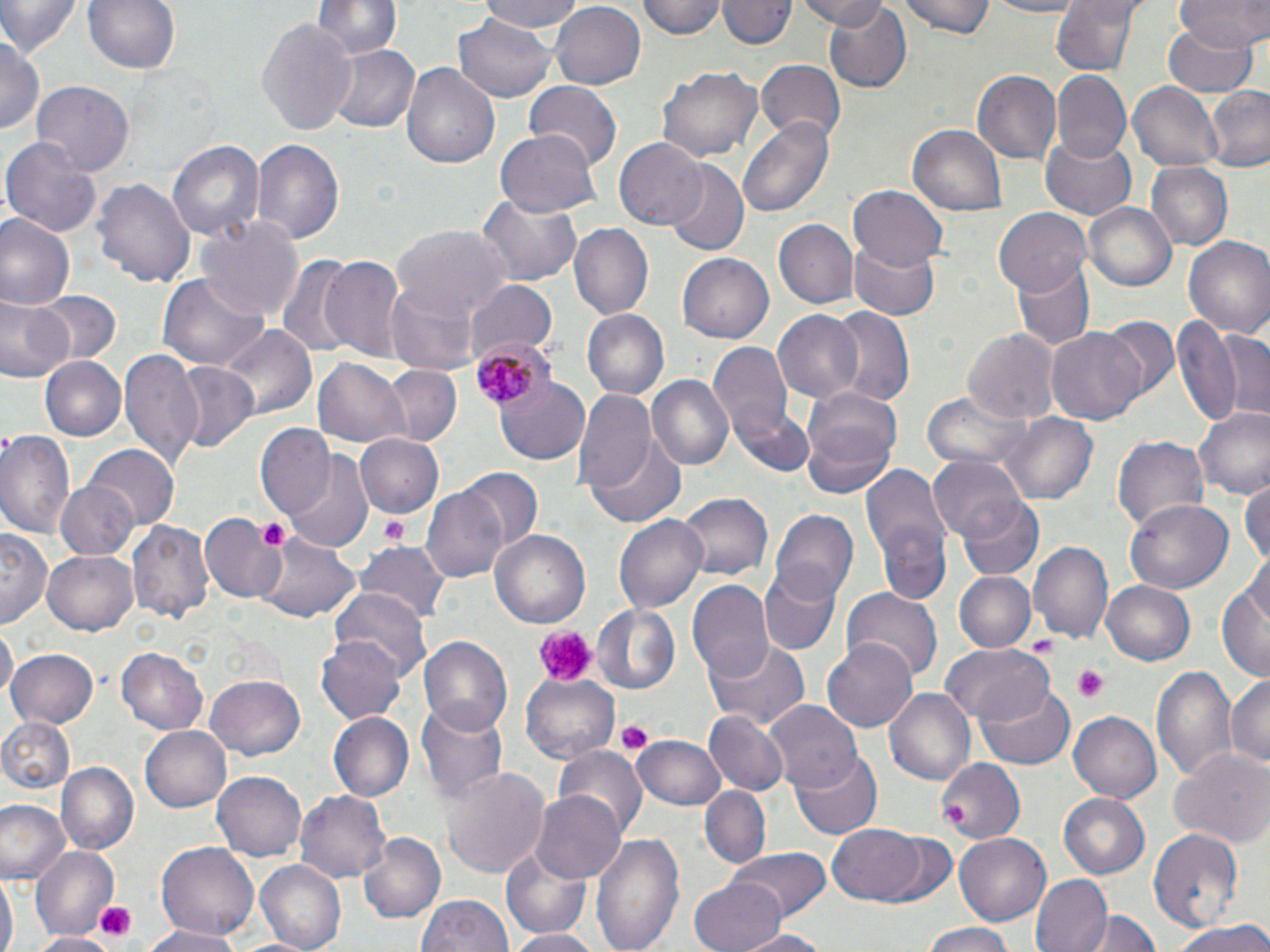

Summary:
  - Coordinate format: approximate bounding boxes as (x1, y1, x2, y2) in pixels
  - Plasmodium malariae-infected red blood cell locations: (468, 336, 555, 414)
  - Platelet locations: (379, 514, 409, 544), (258, 518, 292, 551), (531, 624, 597, 689), (1072, 665, 1112, 702), (615, 718, 651, 753), (939, 802, 964, 826), (93, 901, 136, 943)
  - Uninfected red blood cell locations: (0, 0, 81, 59), (83, 0, 182, 78), (478, 0, 588, 32), (549, 0, 645, 87), (640, 0, 727, 39), (793, 0, 896, 29), (819, 0, 912, 91), (900, 0, 997, 40), (984, 0, 1086, 18), (1053, 0, 1139, 78), (1178, 0, 1269, 48), (313, 1, 400, 62), (719, 1, 792, 52), (452, 13, 555, 102), (258, 19, 356, 135), (1161, 22, 1258, 94), (0, 34, 43, 138), (326, 42, 418, 134), (400, 60, 502, 169), (755, 61, 846, 144), (656, 66, 763, 164), (973, 70, 1064, 166), (1051, 72, 1129, 165), (32, 80, 136, 175), (523, 80, 621, 172), (1128, 80, 1225, 173), (1202, 86, 1270, 173), (737, 117, 835, 219), (909, 124, 1007, 218), (496, 127, 599, 217), (1040, 133, 1139, 218), (4, 134, 103, 238), (167, 137, 264, 244), (249, 137, 344, 248), (614, 138, 707, 230), (663, 161, 749, 253), (1147, 164, 1232, 249), (95, 175, 193, 290), (849, 186, 948, 270), (477, 195, 582, 287), (1085, 202, 1175, 292), (993, 208, 1091, 295), (0, 215, 74, 310), (195, 216, 305, 323), (773, 219, 859, 310), (567, 223, 653, 318), (393, 225, 512, 318), (1182, 235, 1270, 338), (849, 238, 940, 319), (676, 253, 772, 342), (275, 255, 358, 358), (321, 256, 407, 364), (1010, 258, 1094, 350), (158, 273, 268, 371), (387, 282, 483, 375), (466, 283, 559, 363), (34, 289, 118, 365), (0, 295, 72, 386), (827, 304, 915, 407), (580, 310, 670, 401), (772, 310, 865, 404), (1099, 317, 1180, 404), (1173, 317, 1247, 428), (218, 325, 315, 417), (1045, 325, 1146, 426), (961, 327, 1058, 426), (1214, 327, 1269, 424), (709, 343, 794, 443), (120, 350, 205, 470), (313, 356, 409, 448), (41, 357, 126, 441), (171, 363, 259, 455), (379, 364, 462, 447), (646, 374, 734, 472), (493, 376, 591, 466), (574, 390, 656, 497), (801, 391, 900, 498), (924, 391, 1029, 474), (728, 402, 815, 481), (1194, 406, 1270, 502), (997, 412, 1101, 505), (254, 425, 334, 519), (0, 428, 78, 543), (1112, 432, 1210, 533), (355, 434, 445, 518), (587, 434, 688, 528), (86, 445, 180, 532), (284, 454, 373, 554), (929, 456, 1027, 544), (861, 462, 951, 585), (457, 468, 542, 555), (1241, 477, 1270, 567), (56, 480, 140, 560), (421, 484, 513, 587), (674, 492, 770, 582), (958, 495, 1044, 581), (1126, 499, 1233, 596), (770, 509, 858, 607), (202, 514, 286, 603), (613, 515, 708, 614), (126, 517, 214, 624), (874, 521, 952, 608), (491, 527, 593, 629), (0, 528, 52, 624), (256, 535, 359, 625), (1028, 542, 1114, 646), (358, 544, 451, 628), (44, 551, 136, 635), (1220, 563, 1269, 684), (758, 565, 842, 656), (953, 571, 1035, 654), (1102, 580, 1195, 666), (687, 581, 775, 680), (843, 585, 942, 684), (332, 586, 431, 677), (592, 603, 681, 694), (2, 625, 17, 700), (316, 634, 406, 725), (705, 636, 811, 731), (418, 637, 513, 735), (822, 637, 917, 733), (940, 642, 1054, 724), (7, 646, 100, 731), (116, 648, 208, 735), (1151, 665, 1238, 780), (520, 671, 620, 764), (1226, 672, 1269, 773), (205, 676, 307, 759), (975, 682, 1074, 770), (885, 689, 975, 786), (416, 699, 508, 801), (764, 699, 863, 794), (706, 710, 788, 795), (1069, 711, 1161, 802), (327, 713, 414, 802), (0, 718, 76, 794), (140, 725, 233, 812), (632, 734, 727, 810), (554, 744, 645, 836), (1169, 747, 1270, 848), (791, 752, 882, 839), (935, 758, 1025, 845), (58, 761, 137, 852), (441, 768, 549, 876), (211, 771, 307, 861), (697, 787, 772, 870), (296, 789, 390, 886), (530, 790, 626, 884), (1057, 792, 1150, 881), (0, 799, 67, 882), (829, 823, 927, 904), (1148, 827, 1244, 929), (360, 830, 445, 924), (869, 830, 961, 909), (589, 833, 684, 952), (956, 834, 1050, 922), (155, 843, 260, 940), (32, 846, 118, 936), (728, 847, 833, 921), (499, 849, 592, 940), (254, 861, 345, 950), (1, 874, 16, 952), (1029, 874, 1112, 952), (688, 875, 785, 952), (415, 893, 515, 952), (1091, 910, 1161, 952), (1167, 921, 1270, 952), (922, 922, 1015, 952), (143, 927, 250, 951), (731, 928, 835, 951), (505, 929, 600, 952), (29, 932, 120, 952)
  - Slide-level diagnosis: Plasmodium malariae
  - Modality: light microscopy
  - Magnification: 1000x
  - Field of view: one of a larger specimen
  - Preparation: thin blood film
  - Image size: 1270×952 pixels
  - Stain: May-Grünwald-Giemsa